Classify this cell by malaria status.
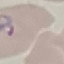

Parasitized.

Summary:
  - Capture: smartphone camera at the microscope eyepiece
  - Preparation: thin blood film
  - Image type: cell patch, automatically extracted from a larger field of view and resized to 64 × 64 pixels
  - Stain: Giemsa